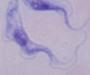
Captured at 1000x magnification. Photomicrograph. A trypanosome is seen.